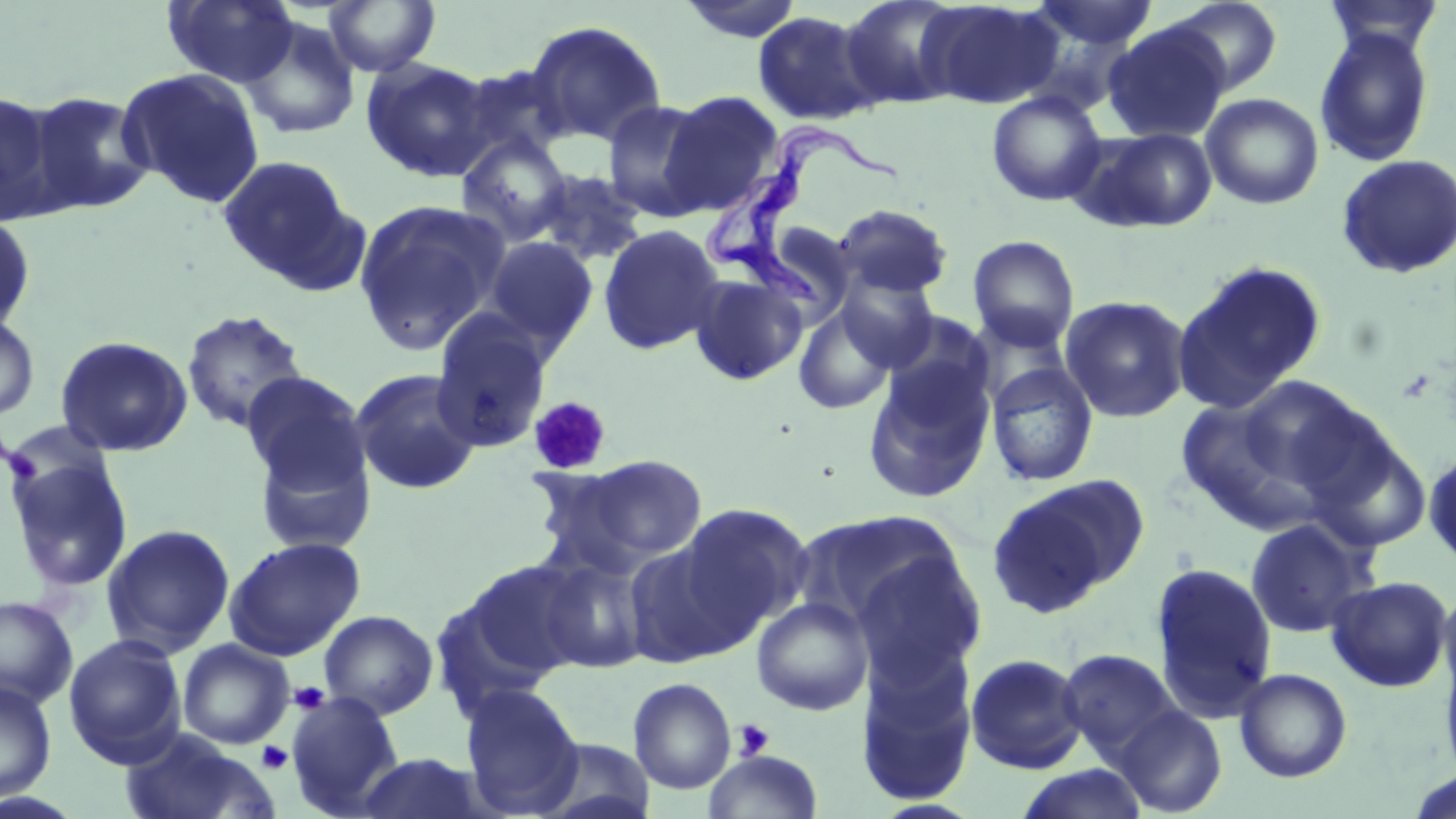

slide-level diagnosis = Trypanosoma brucei
preparation = thin blood film
stain = May-Grünwald-Giemsa
field of view = single
magnification = 1000x
platelet locations = approximate bounding boxes as (x1,y1)-(x2,y2) corner pairs in pixels: (527,396)-(612,475), (289,681)-(330,714), (734,719)-(774,761), (257,741)-(293,773)
image size = 1456×819 pixels
uninfected red blood cell locations = approximate bounding boxes as (x1,y1)-(x2,y2) corner pairs in pixels: (163,0)-(299,87), (323,0)-(441,77), (839,0)-(970,109), (919,1)-(1064,110), (1026,1)-(1160,52), (1163,1)-(1284,97), (1320,1)-(1446,58), (752,10)-(882,126), (240,18)-(360,141), (524,19)-(667,148), (1102,23)-(1230,143), (1315,27)-(1435,167), (362,57)-(496,182), (116,68)-(266,208), (986,90)-(1107,206), (0,91)-(64,225), (26,91)-(154,214), (660,91)-(784,213), (1201,92)-(1324,209), (602,101)-(714,221), (1073,125)-(1220,233), (456,132)-(573,246), (217,154)-(360,290), (1335,154)-(1456,279), (528,169)-(649,268), (353,198)-(510,355), (831,204)-(953,299), (0,214)-(36,334), (598,224)-(724,356), (968,235)-(1080,350), (482,236)-(599,349), (1173,261)-(1327,410), (688,273)-(808,386), (835,274)-(940,371), (1060,295)-(1191,423), (793,304)-(897,416), (181,309)-(309,433), (430,313)-(552,453), (0,314)-(39,422), (877,315)-(992,429), (55,335)-(193,456), (986,362)-(1099,486), (863,365)-(994,503), (350,368)-(482,496), (241,369)-(373,512), (1235,376)-(1378,498), (1171,397)-(1313,526), (1,419)-(117,502), (1305,427)-(1432,552), (1424,447)-(1456,569), (4,451)-(133,594), (541,456)-(709,574), (988,475)-(1146,616), (675,503)-(812,635), (1244,517)-(1376,638), (101,523)-(235,658), (223,536)-(365,660), (623,541)-(747,668), (851,548)-(987,687), (534,554)-(652,674), (462,559)-(593,681), (1149,562)-(1277,721), (1325,575)-(1453,691), (1437,581)-(1456,702), (0,595)-(78,710), (751,597)-(873,716), (319,610)-(438,719), (63,634)-(187,766), (177,639)-(294,749), (857,649)-(979,807), (1057,649)-(1181,760), (1439,649)-(1456,785), (965,653)-(1088,773), (1234,668)-(1353,783), (628,678)-(737,795), (0,679)-(57,803), (459,684)-(585,816), (286,693)-(405,817), (1112,705)-(1228,817), (117,730)-(280,819), (531,737)-(657,819), (704,749)-(822,818), (353,752)-(495,819), (1015,764)-(1150,819), (1404,767)-(1456,819)
modality = optical microscopy
Trypanosoma brucei locations = approximate bounding boxes as (x1,y1)-(x2,y2) corner pairs in pixels: (697,117)-(902,315)